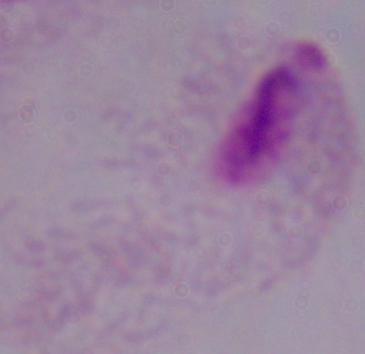 A trichomonad is shown. Photomicrograph. Captured at 1000x magnification.